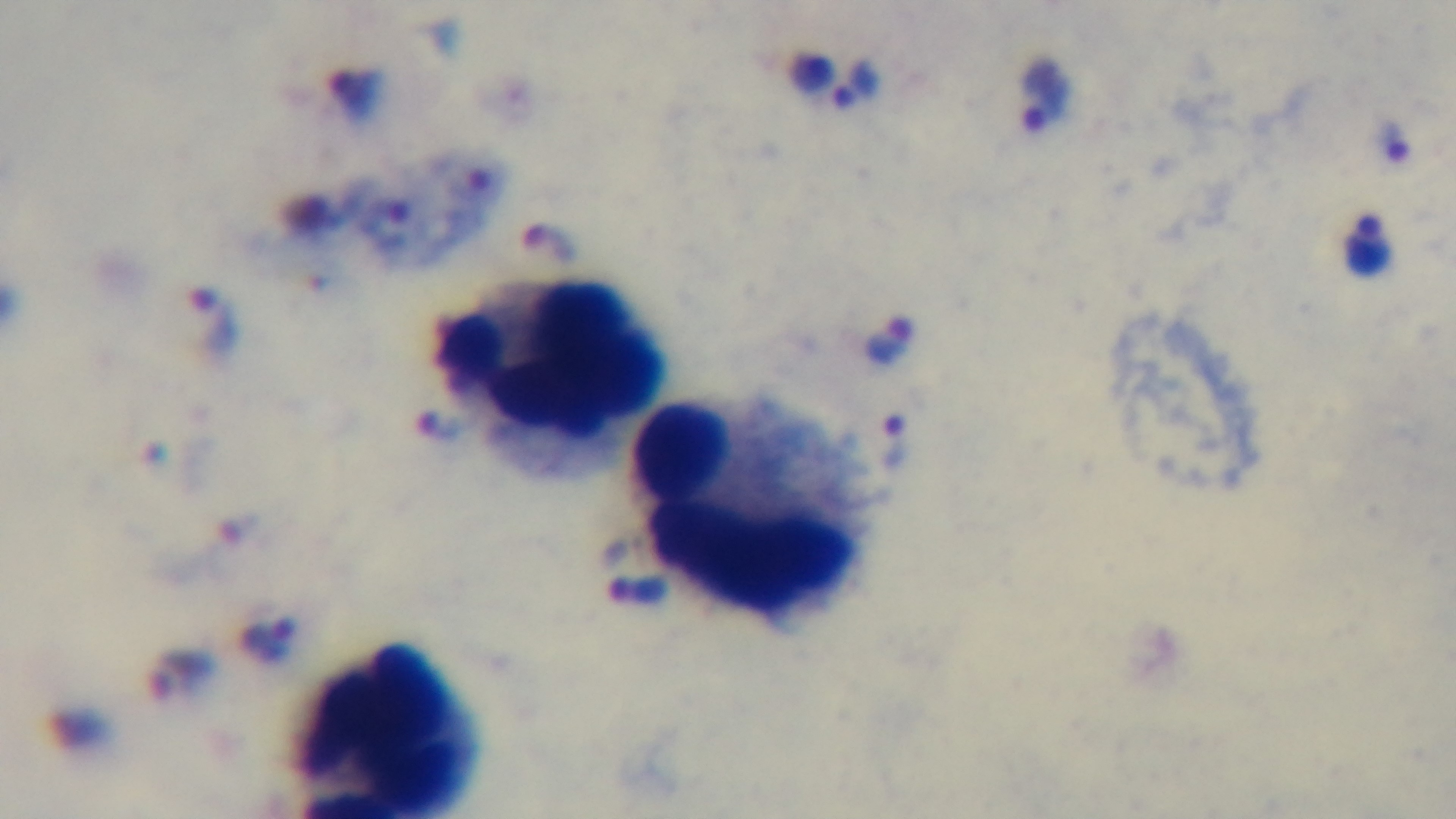

Summary:
  - Malaria status: infected
  - Preparation: thick blood film
  - Stain: Giemsa
  - Field of view: single
  - Modality: light microscopy
  - Objective: 100x oil immersion
  - Capture: mounted 4K digital camera